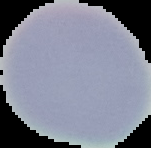

Summary:
  - Preparation: thin blood film
  - Image size: 151×148 pixels
  - Image type: segmented cell region with the area outside set to black
  - Malaria status: uninfected